Assess this cell for malaria.
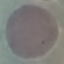
Uninfected.

capture = smartphone camera at the microscope eyepiece
stain = Giemsa
preparation = thin smear
image type = automatically extracted cell patch, resized to 64 × 64 pixels